Describe the morphology of the erythrocytes.
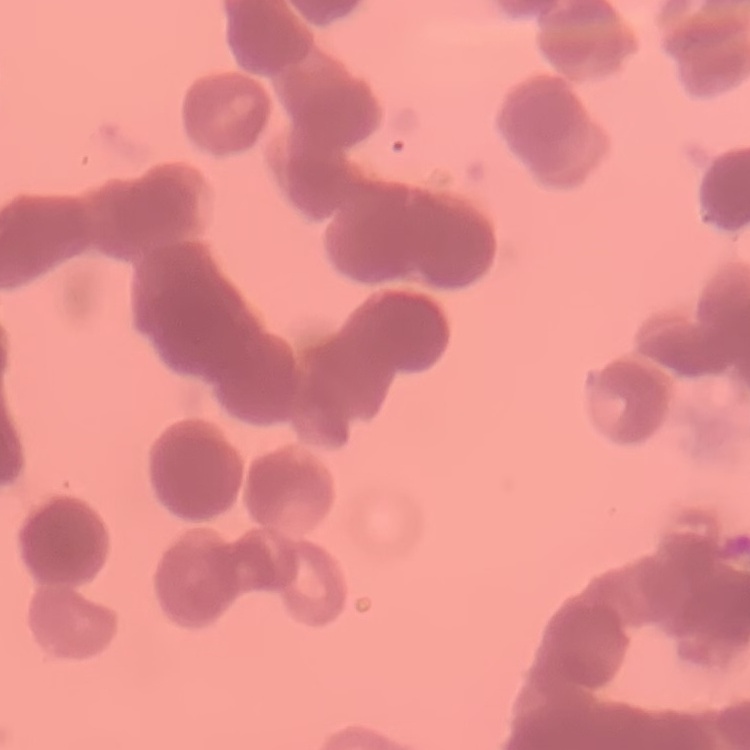
They show rouleaux formation.

Thin blood film. Square crop of a larger photomicrograph. Stained with either Field's or Giemsa.